Identify the cell.
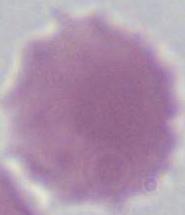

This is an erythrocyte.

Captured at 1000x magnification. Photomicrograph.